Describe the morphology of the erythrocytes.
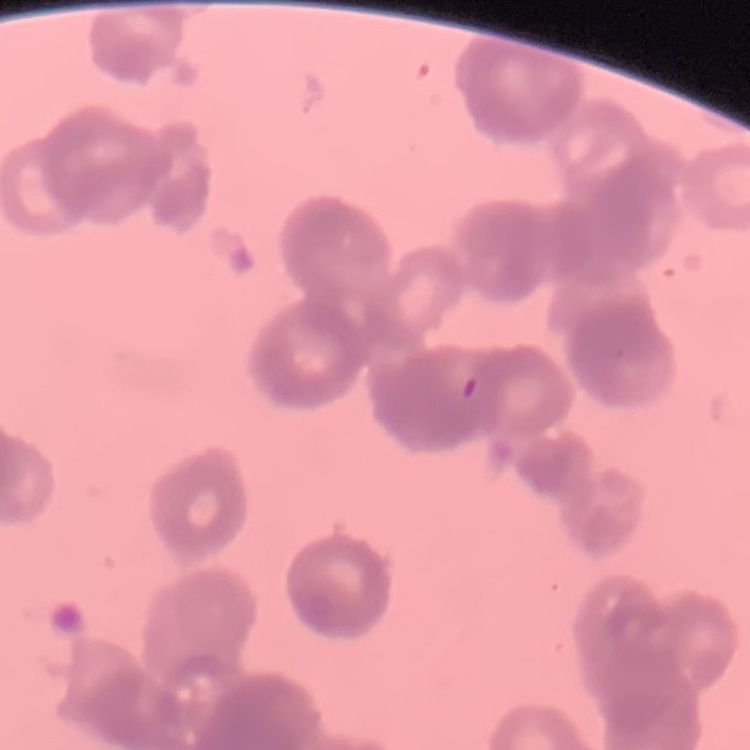

Rouleaux formation.

preparation = thin blood smear
image type = square crop of a larger photomicrograph
stain = Field's or Giemsa